Assess this cell for malaria.
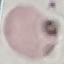
It is uninfected.

Acquired by smartphone through the microscope eyepiece. Thin blood smear. Automatically extracted cell patch, resized to 64 × 64 pixels. Giemsa-stained preparation.